State the blood parasite species.
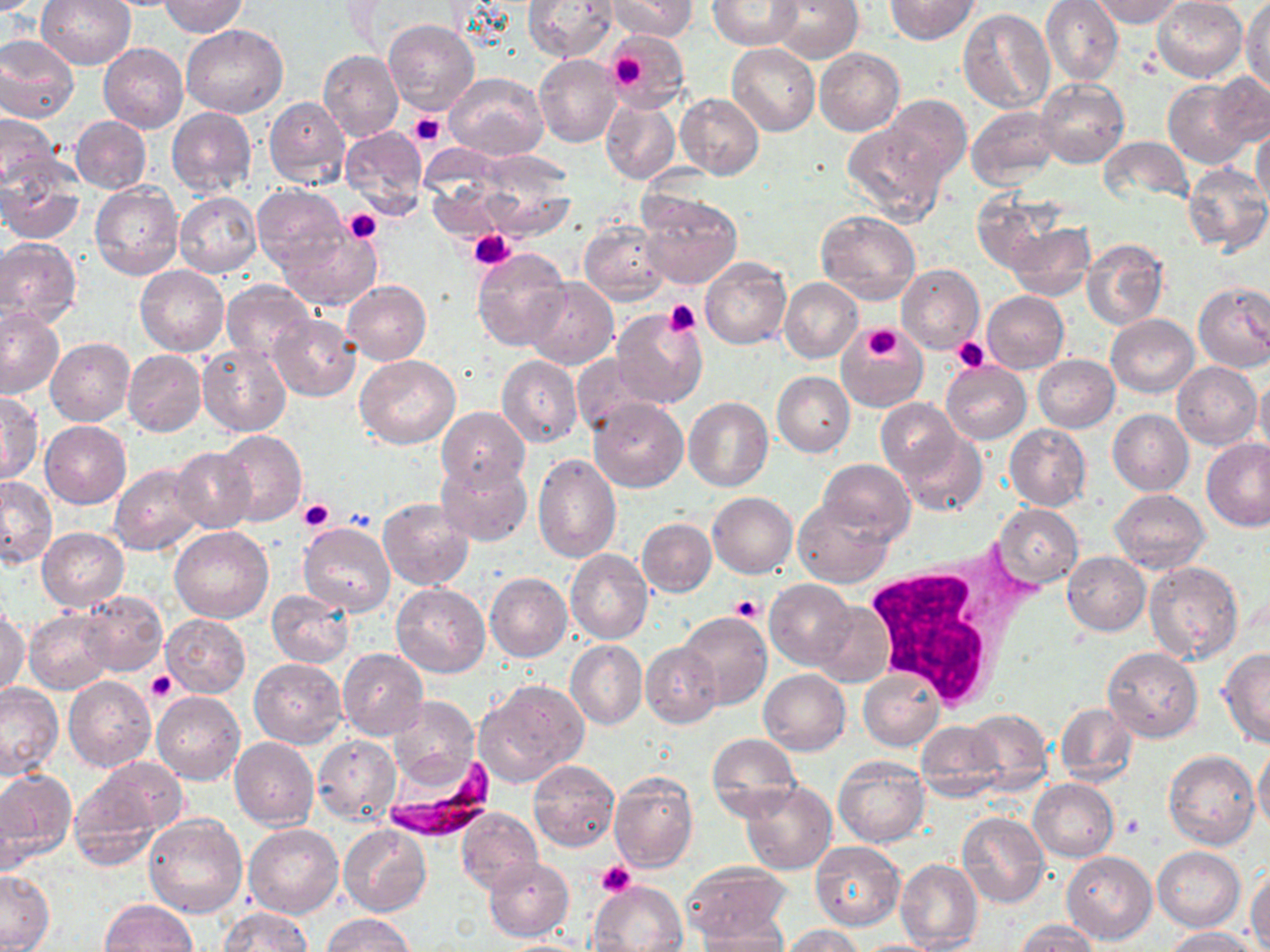
Plasmodium falciparum.

Approximate bounding boxes as named x1/y1/x2/y2 corners in pixels. Uninfected red blood cell locations: (x1=37, y1=0, x2=136, y2=70), (x1=160, y1=0, x2=248, y2=38), (x1=522, y1=0, x2=618, y2=61), (x1=608, y1=0, x2=695, y2=41), (x1=769, y1=0, x2=863, y2=63), (x1=885, y1=0, x2=980, y2=44), (x1=1041, y1=0, x2=1123, y2=85), (x1=1091, y1=0, x2=1184, y2=26), (x1=1152, y1=0, x2=1249, y2=83), (x1=1243, y1=0, x2=1270, y2=92), (x1=708, y1=1, x2=803, y2=50), (x1=958, y1=7, x2=1054, y2=112), (x1=382, y1=19, x2=479, y2=114), (x1=181, y1=22, x2=287, y2=118), (x1=605, y1=28, x2=688, y2=106), (x1=0, y1=35, x2=81, y2=123), (x1=100, y1=43, x2=189, y2=133), (x1=727, y1=43, x2=819, y2=136), (x1=815, y1=48, x2=905, y2=135), (x1=318, y1=50, x2=403, y2=141), (x1=534, y1=54, x2=622, y2=147), (x1=445, y1=71, x2=548, y2=159), (x1=1208, y1=72, x2=1270, y2=147), (x1=1164, y1=78, x2=1255, y2=168), (x1=1036, y1=79, x2=1129, y2=168), (x1=675, y1=93, x2=764, y2=179), (x1=263, y1=96, x2=349, y2=189), (x1=600, y1=96, x2=680, y2=185), (x1=884, y1=96, x2=971, y2=180), (x1=967, y1=106, x2=1059, y2=187), (x1=166, y1=107, x2=256, y2=198), (x1=0, y1=113, x2=62, y2=190), (x1=72, y1=116, x2=151, y2=194), (x1=843, y1=119, x2=950, y2=225), (x1=340, y1=126, x2=427, y2=209), (x1=1252, y1=127, x2=1270, y2=209), (x1=1098, y1=137, x2=1194, y2=206), (x1=0, y1=161, x2=86, y2=244), (x1=1182, y1=163, x2=1270, y2=255), (x1=91, y1=182, x2=183, y2=279), (x1=252, y1=184, x2=348, y2=274), (x1=637, y1=190, x2=742, y2=290), (x1=175, y1=192, x2=261, y2=277), (x1=971, y1=194, x2=1053, y2=274), (x1=816, y1=210, x2=920, y2=305), (x1=580, y1=220, x2=670, y2=306), (x1=1004, y1=221, x2=1095, y2=301), (x1=282, y1=228, x2=379, y2=309), (x1=0, y1=238, x2=82, y2=328), (x1=1082, y1=239, x2=1168, y2=330), (x1=472, y1=247, x2=570, y2=350), (x1=700, y1=257, x2=791, y2=348), (x1=897, y1=263, x2=985, y2=354), (x1=135, y1=264, x2=229, y2=356), (x1=524, y1=278, x2=619, y2=368), (x1=779, y1=278, x2=862, y2=364), (x1=342, y1=279, x2=432, y2=365), (x1=221, y1=280, x2=315, y2=365), (x1=1193, y1=282, x2=1270, y2=373), (x1=983, y1=291, x2=1069, y2=373), (x1=0, y1=305, x2=66, y2=398), (x1=611, y1=309, x2=709, y2=410), (x1=268, y1=313, x2=360, y2=401), (x1=1106, y1=314, x2=1198, y2=397), (x1=838, y1=328, x2=928, y2=411), (x1=46, y1=338, x2=135, y2=426), (x1=198, y1=343, x2=291, y2=436), (x1=121, y1=350, x2=206, y2=436), (x1=571, y1=354, x2=651, y2=438), (x1=1033, y1=354, x2=1119, y2=432), (x1=498, y1=355, x2=583, y2=447), (x1=355, y1=356, x2=461, y2=448), (x1=1173, y1=361, x2=1261, y2=449), (x1=941, y1=362, x2=1030, y2=443), (x1=1255, y1=371, x2=1270, y2=461), (x1=772, y1=372, x2=855, y2=457), (x1=0, y1=391, x2=43, y2=485), (x1=684, y1=397, x2=773, y2=491), (x1=589, y1=398, x2=687, y2=492), (x1=876, y1=399, x2=962, y2=483), (x1=437, y1=406, x2=529, y2=495), (x1=1108, y1=409, x2=1194, y2=494), (x1=41, y1=421, x2=131, y2=509), (x1=1004, y1=423, x2=1092, y2=510), (x1=896, y1=427, x2=987, y2=517), (x1=215, y1=430, x2=307, y2=527), (x1=1200, y1=439, x2=1270, y2=531), (x1=171, y1=446, x2=257, y2=533), (x1=532, y1=453, x2=621, y2=563), (x1=438, y1=457, x2=532, y2=546), (x1=818, y1=459, x2=914, y2=543), (x1=109, y1=464, x2=207, y2=556), (x1=1, y1=475, x2=56, y2=565), (x1=1110, y1=487, x2=1210, y2=573), (x1=708, y1=492, x2=798, y2=578), (x1=377, y1=497, x2=473, y2=589), (x1=793, y1=499, x2=891, y2=588), (x1=993, y1=503, x2=1083, y2=588), (x1=637, y1=518, x2=717, y2=597), (x1=297, y1=523, x2=396, y2=616), (x1=169, y1=525, x2=274, y2=623), (x1=38, y1=528, x2=129, y2=612), (x1=565, y1=549, x2=653, y2=644), (x1=1062, y1=552, x2=1150, y2=635), (x1=1144, y1=560, x2=1245, y2=666), (x1=485, y1=572, x2=572, y2=661), (x1=766, y1=579, x2=858, y2=668), (x1=390, y1=583, x2=490, y2=678), (x1=76, y1=590, x2=168, y2=676), (x1=267, y1=590, x2=355, y2=668), (x1=811, y1=601, x2=894, y2=688), (x1=0, y1=608, x2=30, y2=698), (x1=25, y1=611, x2=115, y2=694), (x1=677, y1=612, x2=773, y2=711), (x1=161, y1=613, x2=252, y2=696), (x1=566, y1=640, x2=647, y2=729), (x1=641, y1=642, x2=722, y2=726), (x1=1101, y1=646, x2=1203, y2=742), (x1=1218, y1=648, x2=1270, y2=747), (x1=337, y1=649, x2=428, y2=739), (x1=250, y1=658, x2=346, y2=747), (x1=759, y1=668, x2=850, y2=755), (x1=859, y1=668, x2=944, y2=751), (x1=64, y1=677, x2=156, y2=772), (x1=476, y1=680, x2=589, y2=786), (x1=0, y1=684, x2=65, y2=781), (x1=152, y1=691, x2=244, y2=784), (x1=388, y1=696, x2=479, y2=790), (x1=1055, y1=703, x2=1137, y2=786), (x1=964, y1=708, x2=1052, y2=794), (x1=914, y1=721, x2=1005, y2=799), (x1=706, y1=734, x2=800, y2=820), (x1=230, y1=736, x2=319, y2=828), (x1=312, y1=737, x2=401, y2=825), (x1=1254, y1=743, x2=1270, y2=835), (x1=1164, y1=750, x2=1259, y2=850), (x1=833, y1=756, x2=929, y2=847), (x1=89, y1=757, x2=187, y2=837), (x1=528, y1=760, x2=620, y2=852), (x1=0, y1=770, x2=74, y2=864), (x1=609, y1=771, x2=698, y2=873), (x1=70, y1=773, x2=167, y2=869), (x1=1028, y1=779, x2=1119, y2=862), (x1=740, y1=781, x2=838, y2=875), (x1=2, y1=785, x2=33, y2=876), (x1=454, y1=808, x2=543, y2=893), (x1=957, y1=812, x2=1050, y2=908), (x1=143, y1=814, x2=247, y2=919), (x1=244, y1=822, x2=343, y2=918), (x1=339, y1=823, x2=431, y2=915), (x1=810, y1=841, x2=905, y2=929), (x1=1153, y1=846, x2=1245, y2=931), (x1=1061, y1=851, x2=1156, y2=945), (x1=484, y1=857, x2=573, y2=941), (x1=896, y1=858, x2=983, y2=952), (x1=681, y1=862, x2=793, y2=945), (x1=1248, y1=867, x2=1270, y2=950), (x1=0, y1=869, x2=53, y2=952), (x1=590, y1=880, x2=686, y2=952), (x1=102, y1=900, x2=196, y2=952), (x1=218, y1=907, x2=311, y2=951), (x1=322, y1=913, x2=416, y2=952), (x1=696, y1=921, x2=791, y2=951), (x1=1016, y1=921, x2=1101, y2=951), (x1=779, y1=924, x2=869, y2=951), (x1=1165, y1=927, x2=1261, y2=951), (x1=495, y1=938, x2=600, y2=951), (x1=849, y1=939, x2=951, y2=951). White blood cell locations: (x1=864, y1=551, x2=1031, y2=711). Plasmodium falciparum-infected red blood cell locations: (x1=382, y1=748, x2=495, y2=839). Platelet locations: (x1=609, y1=51, x2=652, y2=91), (x1=409, y1=112, x2=446, y2=147), (x1=343, y1=208, x2=382, y2=244), (x1=469, y1=230, x2=513, y2=269), (x1=664, y1=298, x2=701, y2=336), (x1=847, y1=321, x2=916, y2=375), (x1=863, y1=324, x2=906, y2=362), (x1=952, y1=336, x2=991, y2=375), (x1=298, y1=500, x2=335, y2=532), (x1=730, y1=594, x2=765, y2=624), (x1=147, y1=671, x2=178, y2=702), (x1=597, y1=861, x2=636, y2=897). Thin blood film. May-Grünwald-Giemsa-stained preparation. Optical microscopy. 1000x magnification. Single field of view. Image is 1270×952 pixels.